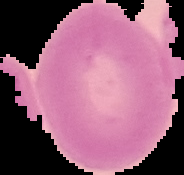 The area outside the segmented cell region is set to black. Malaria status: uninfected. Image is 184×175 pixels. From a thin blood film.